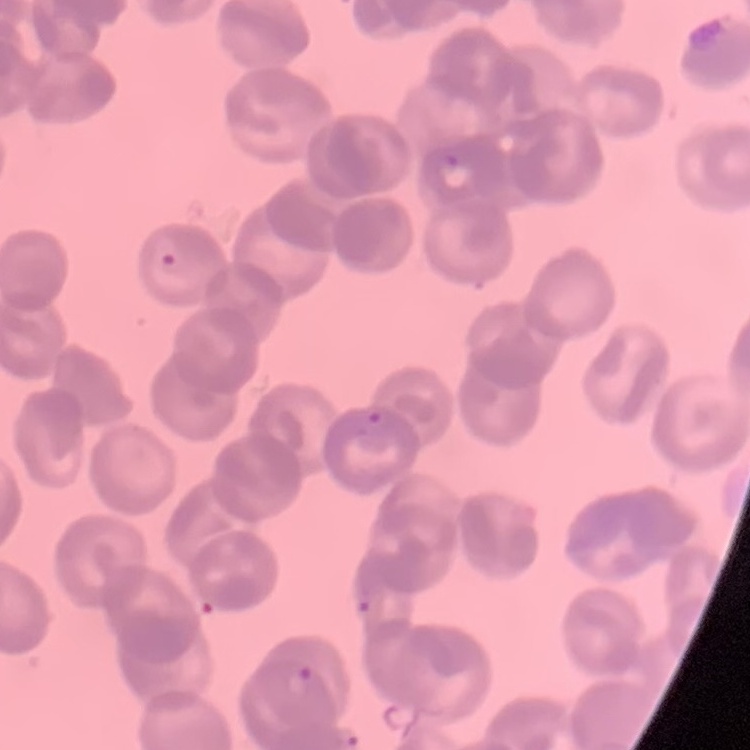

Summary:
  - Red blood cell morphology: rouleaux formation
  - Image type: one tile cut from a larger photomicrograph
  - Preparation: thin blood film
  - Stain: Field's or Giemsa